Locate every Plasmodium falciparum-infected red blood cell.
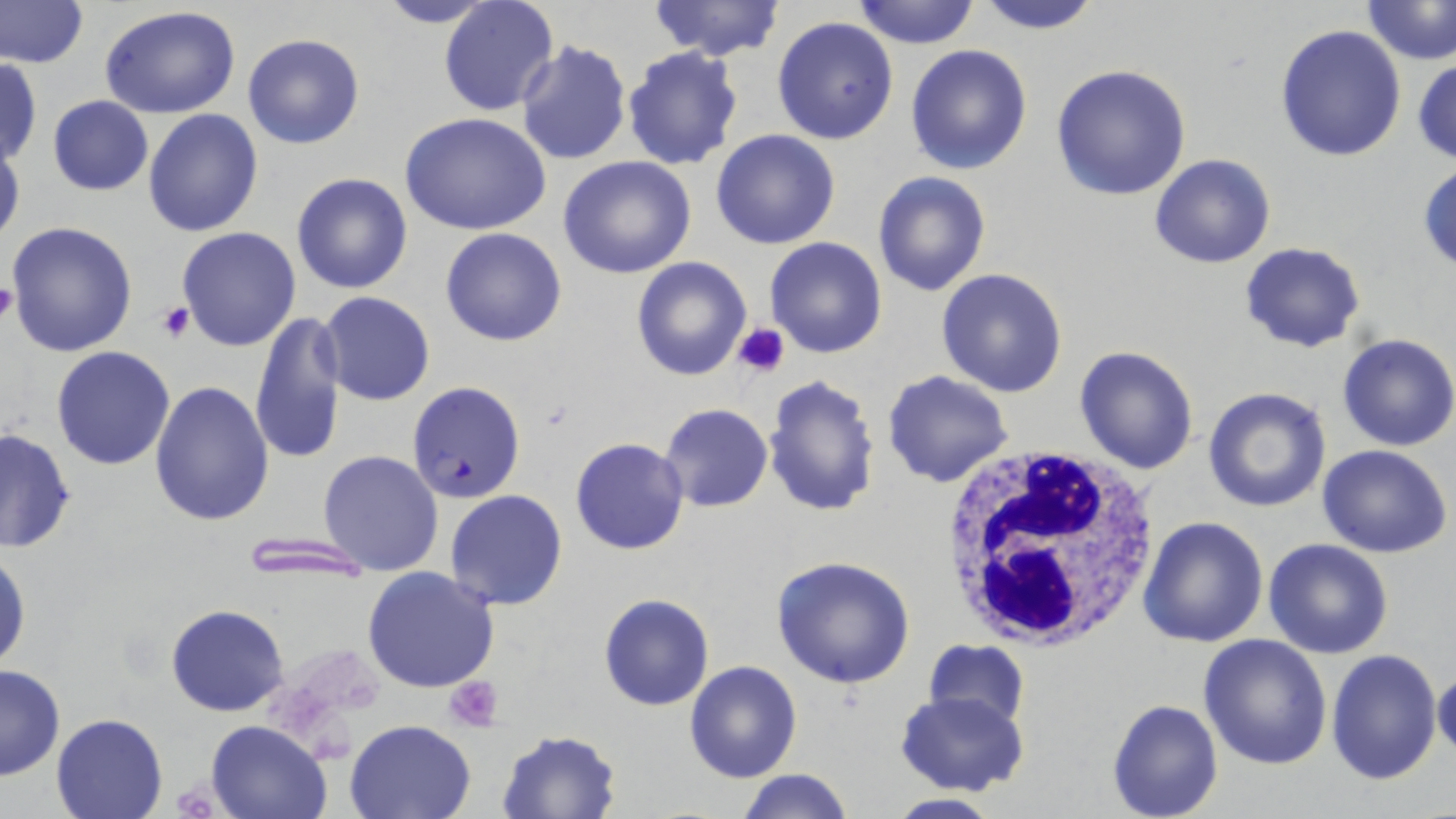

Approximate bounding boxes as (x1, y1, x2, y2) in pixels.
Plasmodium falciparum-infected red blood cells: (406, 380, 528, 504).

Summary:
  - Platelet locations: (0, 280, 17, 325), (157, 300, 195, 340), (732, 323, 791, 377), (444, 674, 505, 731), (169, 780, 224, 818)
  - White blood cell locations: (938, 441, 1162, 654)
  - Uninfected red blood cell locations: (371, 0, 498, 27), (438, 0, 560, 119), (649, 0, 783, 62), (851, 0, 981, 49), (973, 0, 1104, 34), (0, 1, 87, 69), (1363, 1, 1456, 64), (98, 5, 241, 119), (772, 15, 899, 145), (1275, 24, 1407, 161), (241, 32, 366, 150), (516, 39, 632, 167), (906, 43, 1033, 176), (622, 47, 743, 171), (1413, 54, 1456, 165), (1, 58, 41, 166), (1051, 64, 1192, 199), (47, 95, 153, 196), (142, 108, 264, 238), (399, 112, 551, 235), (710, 130, 840, 249), (0, 133, 25, 250), (1149, 153, 1276, 269), (558, 156, 696, 279), (1419, 162, 1456, 274), (872, 171, 993, 296), (291, 172, 415, 295), (6, 221, 139, 357), (177, 227, 303, 351), (440, 228, 568, 346), (765, 237, 887, 358), (1239, 242, 1365, 353), (631, 256, 752, 381), (937, 267, 1070, 396), (317, 292, 435, 406), (251, 311, 348, 466), (1336, 333, 1456, 452), (1073, 345, 1201, 475), (50, 346, 176, 471), (882, 370, 1013, 488), (762, 375, 882, 518), (149, 380, 274, 526), (1203, 386, 1332, 514), (659, 403, 773, 513), (1, 428, 75, 555), (570, 438, 689, 555), (1317, 444, 1452, 558), (318, 451, 444, 575), (444, 489, 567, 611), (1139, 516, 1269, 649), (239, 534, 372, 578), (1264, 538, 1395, 659), (0, 547, 30, 673), (770, 554, 916, 689), (361, 565, 500, 694), (598, 593, 713, 711), (166, 603, 290, 716), (1197, 634, 1332, 772), (922, 640, 1032, 733), (1326, 648, 1444, 786), (683, 661, 804, 782), (0, 665, 66, 781), (1434, 671, 1456, 756), (897, 691, 1029, 796), (1106, 698, 1223, 819), (51, 714, 167, 819), (205, 718, 331, 818), (344, 719, 478, 818), (496, 729, 621, 818), (737, 768, 853, 819), (880, 793, 1007, 818)
  - Slide-level diagnosis: Plasmodium falciparum
  - Preparation: thin blood smear
  - Image size: 1456×819 pixels
  - Stain: May-Grünwald-Giemsa
  - Magnification: 1000x
  - Modality: optical microscopy
  - Field of view: one of a larger specimen